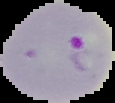

result = Plasmodium parasites detected
image type = cell region segmented out of the field of view; surrounding area masked to black
image size = 115×103 pixels
preparation = thin blood film